Locate every blood parasite and identify its species.
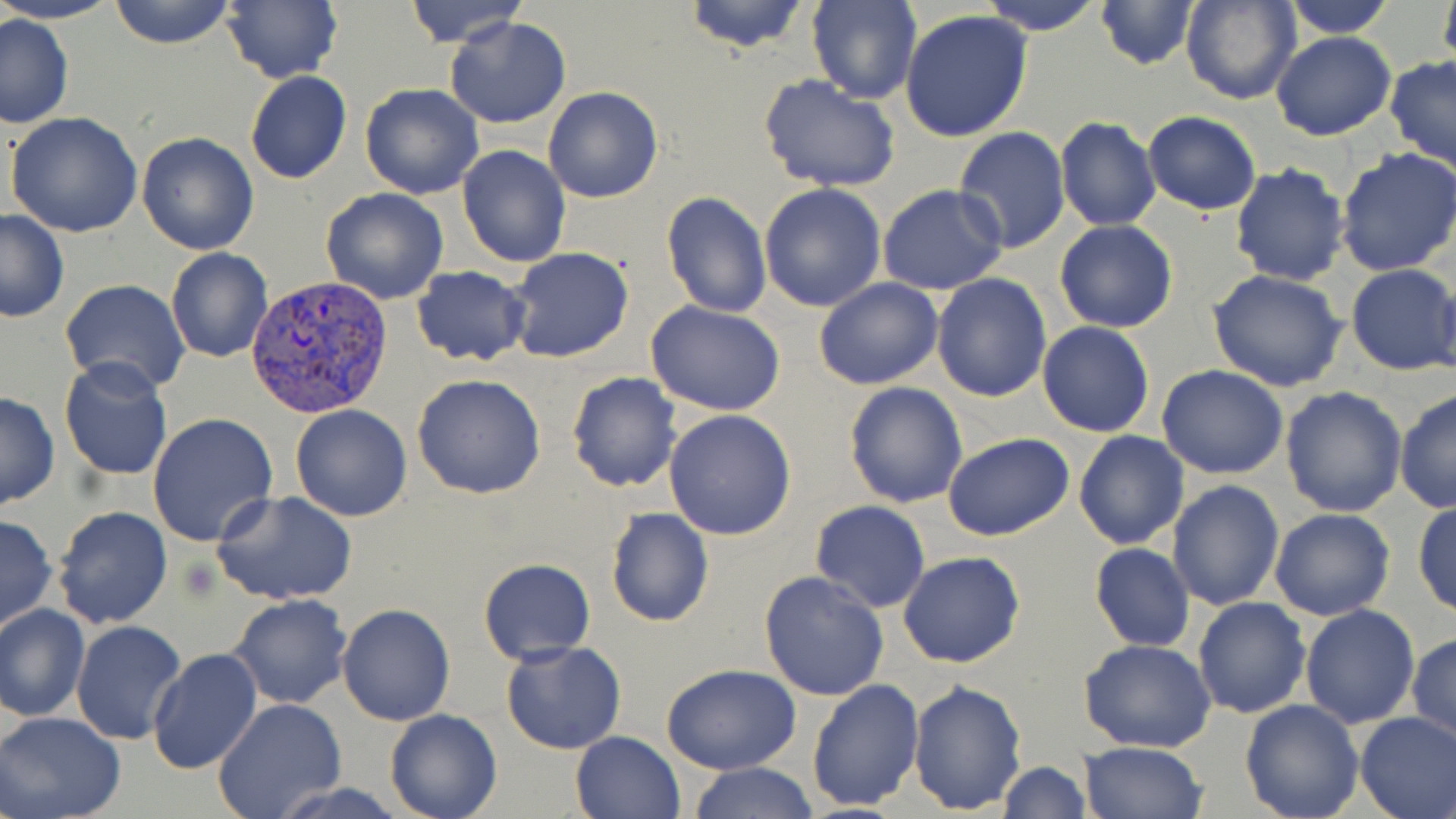

Approximate bounding boxes as named x1/y1/x2/y2 corners in pixels.
Plasmodium vivax-infected red blood cells: (x1=244, y1=275, x2=394, y2=420).
No Plasmodium falciparum, Plasmodium ovale, Plasmodium malariae, Babesia divergens, or Trypanosoma brucei observed.

Summary:
  - Platelet locations: (x1=182, y1=558, x2=222, y2=601)
  - Uninfected red blood cell locations: (x1=0, y1=0, x2=123, y2=25), (x1=109, y1=0, x2=236, y2=48), (x1=221, y1=0, x2=342, y2=84), (x1=401, y1=0, x2=527, y2=48), (x1=681, y1=0, x2=812, y2=53), (x1=978, y1=0, x2=1104, y2=36), (x1=1094, y1=0, x2=1199, y2=71), (x1=1183, y1=0, x2=1301, y2=105), (x1=1279, y1=0, x2=1401, y2=38), (x1=1438, y1=0, x2=1456, y2=70), (x1=806, y1=1, x2=921, y2=103), (x1=901, y1=9, x2=1034, y2=141), (x1=1, y1=14, x2=74, y2=129), (x1=444, y1=16, x2=570, y2=128), (x1=1270, y1=31, x2=1396, y2=141), (x1=1385, y1=55, x2=1456, y2=173), (x1=244, y1=70, x2=352, y2=185), (x1=758, y1=74, x2=900, y2=194), (x1=359, y1=83, x2=483, y2=199), (x1=543, y1=87, x2=664, y2=204), (x1=5, y1=111, x2=143, y2=237), (x1=1142, y1=111, x2=1262, y2=215), (x1=1055, y1=117, x2=1162, y2=232), (x1=953, y1=126, x2=1071, y2=253), (x1=136, y1=131, x2=259, y2=254), (x1=457, y1=144, x2=571, y2=269), (x1=1335, y1=148, x2=1456, y2=279), (x1=1229, y1=164, x2=1350, y2=286), (x1=759, y1=183, x2=887, y2=313), (x1=877, y1=185, x2=1008, y2=296), (x1=321, y1=187, x2=449, y2=305), (x1=660, y1=190, x2=772, y2=318), (x1=0, y1=211, x2=71, y2=323), (x1=1054, y1=221, x2=1179, y2=333), (x1=167, y1=248, x2=273, y2=363), (x1=505, y1=248, x2=634, y2=363), (x1=1347, y1=263, x2=1456, y2=377), (x1=410, y1=265, x2=532, y2=368), (x1=1206, y1=270, x2=1350, y2=392), (x1=931, y1=273, x2=1053, y2=402), (x1=1432, y1=273, x2=1456, y2=387), (x1=823, y1=274, x2=954, y2=502), (x1=813, y1=276, x2=944, y2=390), (x1=61, y1=279, x2=191, y2=394), (x1=645, y1=302, x2=787, y2=418), (x1=1049, y1=318, x2=1165, y2=551), (x1=1038, y1=322, x2=1155, y2=438), (x1=61, y1=357, x2=171, y2=483), (x1=1158, y1=365, x2=1289, y2=479), (x1=566, y1=372, x2=683, y2=493), (x1=411, y1=373, x2=547, y2=500), (x1=843, y1=380, x2=968, y2=507), (x1=1279, y1=387, x2=1407, y2=518), (x1=1395, y1=390, x2=1456, y2=514), (x1=0, y1=392, x2=60, y2=512), (x1=290, y1=404, x2=413, y2=521), (x1=663, y1=409, x2=797, y2=541), (x1=147, y1=412, x2=278, y2=547), (x1=1074, y1=429, x2=1190, y2=549), (x1=943, y1=433, x2=1074, y2=542), (x1=1167, y1=479, x2=1284, y2=611), (x1=211, y1=490, x2=357, y2=606), (x1=1413, y1=499, x2=1456, y2=619), (x1=809, y1=501, x2=930, y2=614), (x1=53, y1=505, x2=174, y2=631), (x1=606, y1=506, x2=714, y2=628), (x1=1269, y1=508, x2=1397, y2=621), (x1=0, y1=515, x2=57, y2=633), (x1=1089, y1=543, x2=1195, y2=652), (x1=898, y1=550, x2=1026, y2=669), (x1=478, y1=557, x2=596, y2=663), (x1=759, y1=569, x2=890, y2=701), (x1=226, y1=594, x2=352, y2=710), (x1=1193, y1=596, x2=1310, y2=718), (x1=0, y1=602, x2=89, y2=722), (x1=336, y1=603, x2=455, y2=725), (x1=1298, y1=604, x2=1420, y2=728), (x1=70, y1=620, x2=188, y2=746), (x1=1407, y1=631, x2=1456, y2=748), (x1=1077, y1=638, x2=1218, y2=753), (x1=500, y1=640, x2=627, y2=755), (x1=147, y1=647, x2=264, y2=774), (x1=659, y1=663, x2=801, y2=775), (x1=807, y1=678, x2=924, y2=811), (x1=909, y1=679, x2=1028, y2=814), (x1=213, y1=699, x2=347, y2=819), (x1=1239, y1=699, x2=1365, y2=819), (x1=385, y1=707, x2=502, y2=819), (x1=0, y1=711, x2=126, y2=819), (x1=1355, y1=712, x2=1456, y2=819), (x1=570, y1=731, x2=687, y2=819), (x1=1079, y1=742, x2=1206, y2=819), (x1=997, y1=761, x2=1090, y2=818), (x1=687, y1=762, x2=819, y2=819), (x1=268, y1=781, x2=409, y2=819)
  - Slide-level diagnosis: Plasmodium vivax
  - Stain: May-Grünwald-Giemsa
  - Preparation: thin blood film
  - Field of view: single
  - Magnification: 1000x
  - Modality: light microscopy
  - Image size: 1456×819 pixels